Assess this cell for malaria.
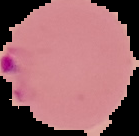

Parasitized.

image_size: 139×136 pixels
preparation: thin blood film
image_type: segmented cell region with the area outside set to black